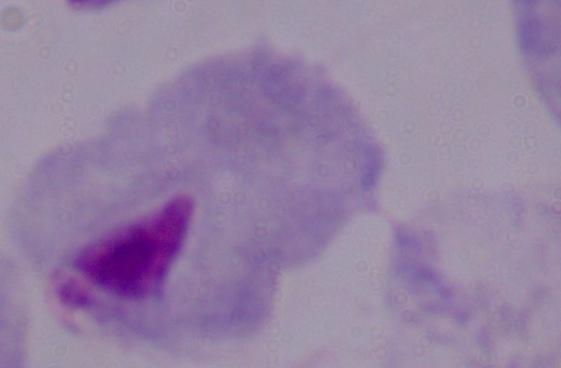 A trichomonad is shown. Photomicrograph. 1000x magnification.